Report the malaria status of this cell.
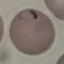

Parasitized.

Summary:
  - Preparation: thin blood smear
  - Image type: cell patch, automatically extracted from a larger field of view and resized to 64 × 64 pixels
  - Stain: Giemsa
  - Capture: smartphone camera at the microscope eyepiece